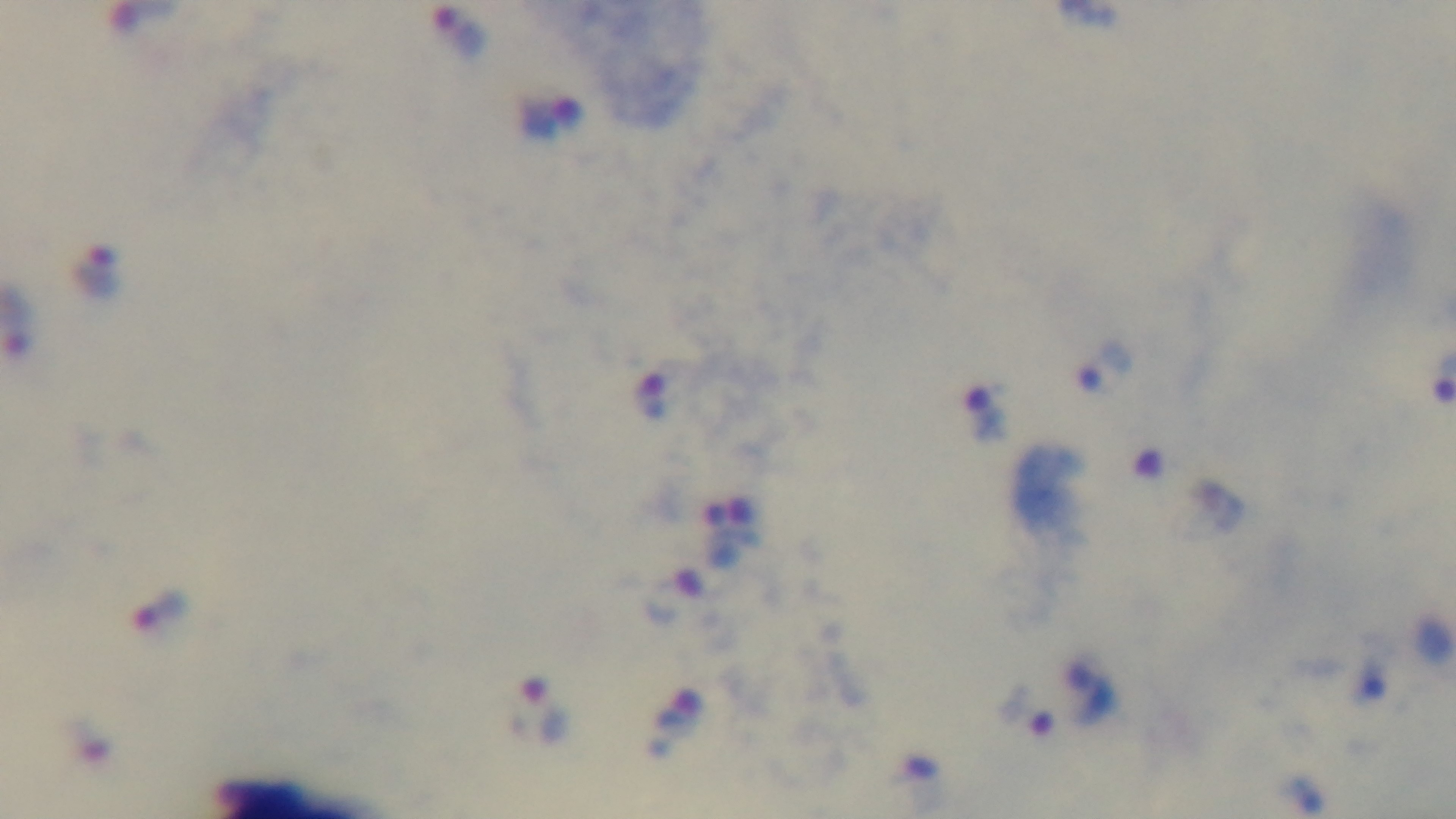

{
  "malaria_status": "infected",
  "stain": "Giemsa",
  "preparation": "thick blood film",
  "modality": "light microscopy",
  "objective": "100x oil immersion",
  "field_of_view": "one from the slide",
  "capture": "mounted 4K digital camera"
}